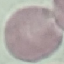

malaria status = uninfected
capture = smartphone camera at the microscope eyepiece
stain = Giemsa
preparation = thin smear
image type = automatically extracted cell patch, resized to 64 × 64 pixels